Locate every uninfected red blood cell.
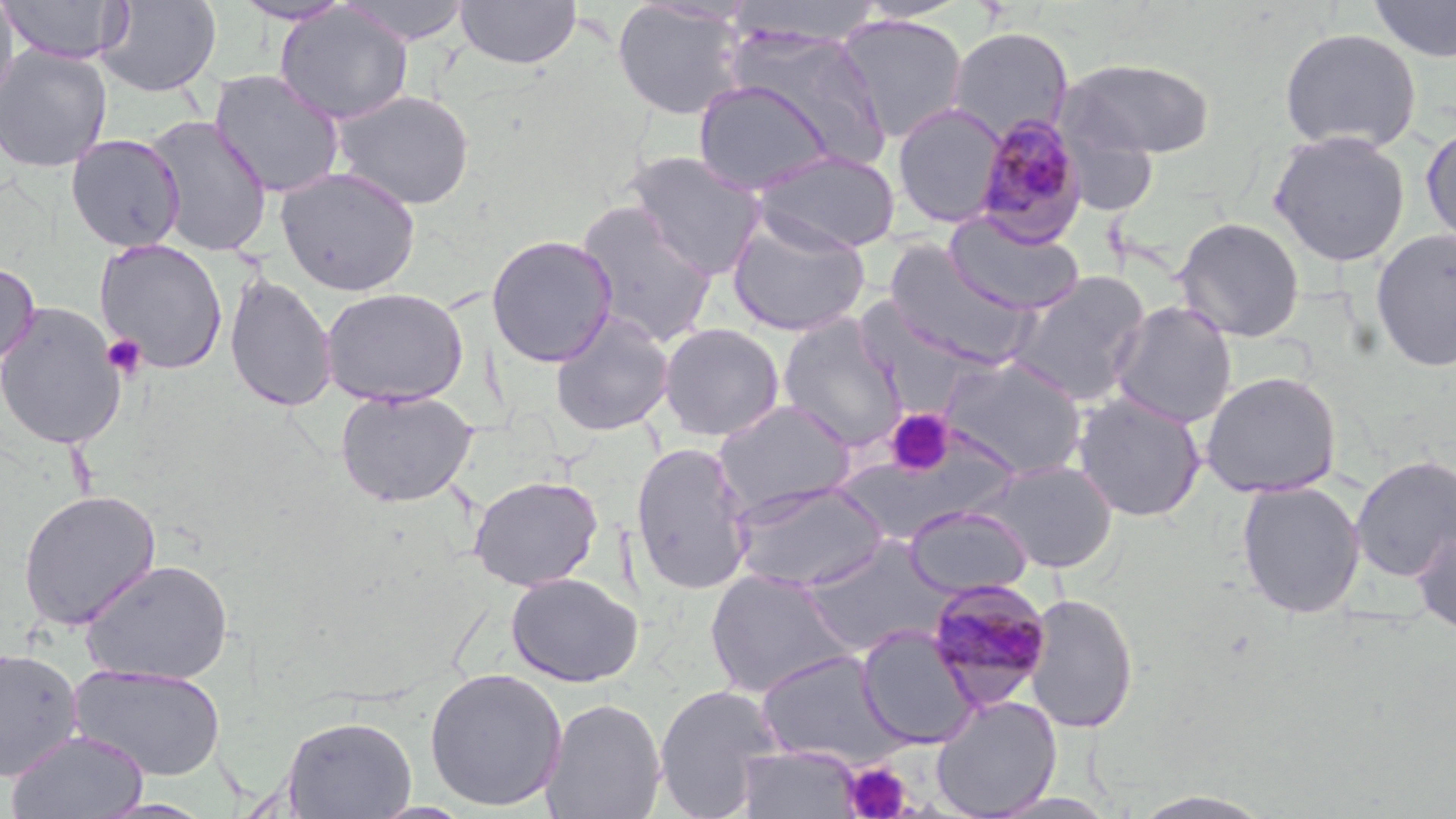

Approximate bounding boxes as (x1,y1)-(x2,y2) corner pairs in pixels.
Uninfected red blood cells: (0,0)-(132,64), (0,0)-(19,115), (233,0)-(354,25), (335,0)-(475,45), (454,0)-(582,70), (1367,0)-(1456,63), (96,1)-(222,97), (610,1)-(749,120), (725,2)-(886,48), (274,4)-(412,125), (835,14)-(969,144), (947,26)-(1074,145), (1278,26)-(1423,154), (720,28)-(891,171), (0,45)-(113,172), (1059,57)-(1217,160), (209,69)-(346,198), (692,79)-(837,195), (330,89)-(476,210), (892,102)-(1007,228), (144,115)-(273,256), (1420,122)-(1455,249), (1268,129)-(1412,267), (66,134)-(185,252), (752,149)-(902,254), (623,150)-(768,279), (275,166)-(421,296), (574,201)-(719,347), (945,213)-(1086,316), (726,214)-(871,337), (1173,216)-(1306,342), (1370,229)-(1456,373), (486,234)-(618,367), (94,239)-(228,374), (885,241)-(1036,366), (0,260)-(40,370), (1006,270)-(1152,406), (223,272)-(337,411), (320,286)-(469,406), (1110,300)-(1238,429), (0,301)-(127,450), (550,310)-(676,437), (777,315)-(908,453), (658,322)-(785,442), (940,355)-(1087,477), (1200,370)-(1343,498), (334,388)-(478,507), (1072,392)-(1206,523), (713,399)-(856,518), (630,441)-(755,596), (1350,453)-(1456,584), (978,459)-(1119,573), (468,474)-(603,591), (1236,480)-(1366,619), (730,481)-(890,593), (18,489)-(161,631), (904,505)-(1033,597), (1411,526)-(1456,636), (799,537)-(953,656), (80,557)-(234,685), (705,568)-(857,699), (506,572)-(643,687), (1023,592)-(1139,734), (857,624)-(981,748), (0,647)-(84,783), (753,649)-(907,767), (68,663)-(227,781), (424,667)-(568,812), (653,683)-(785,818), (931,695)-(1062,818), (541,697)-(667,819), (281,716)-(417,818), (6,729)-(149,818), (736,744)-(864,819), (1128,791)-(1277,818).

slide_level_diagnosis: Plasmodium malariae
platelet_locations: 'approximate bounding boxes as (x1,y1)-(x2,y2) corner pairs in pixels: (102,334)-(147,379), (886,409)-(954,477), (843,760)-(913,819)'
stain: May-Grünwald-Giemsa
image_size: 1456×819 pixels
plasmodium_malariae_infected_red_blood_cell_locations: 'approximate bounding boxes as (x1,y1)-(x2,y2) corner pairs in pixels: (971,115)-(1089,246), (923,577)-(1054,710)'
modality: light microscopy
magnification: 1000x
field_of_view: single
preparation: thin blood film